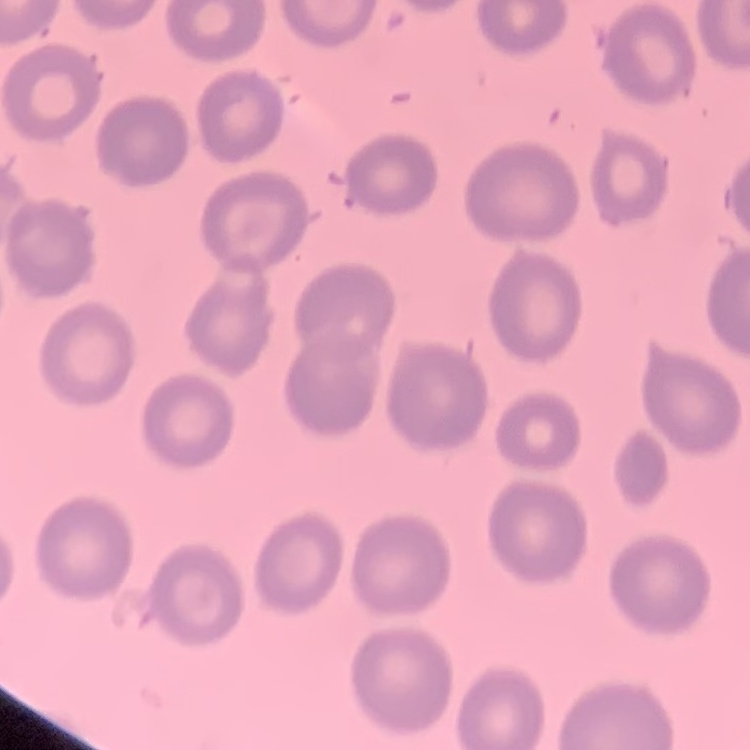

{
  "red_blood_cell_morphology": "no rouleaux formation",
  "image_type": "one tile cut from a larger photomicrograph",
  "preparation": "thin blood smear",
  "stain": "Field's or Giemsa"
}